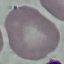

malaria_status: uninfected
stain: Giemsa
capture: smartphone through the microscope eyepiece
preparation: thin blood film
image_type: cell patch, automatically extracted from a larger field of view and resized to 64 × 64 pixels